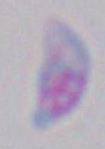

Summary:
  - Identification: Toxoplasma gondii
  - Modality: micrograph
  - Magnification: 1000x